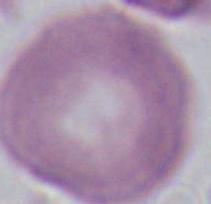

Summary:
  - Modality: photomicrograph
  - Magnification: 1000x
  - Identification: erythrocyte